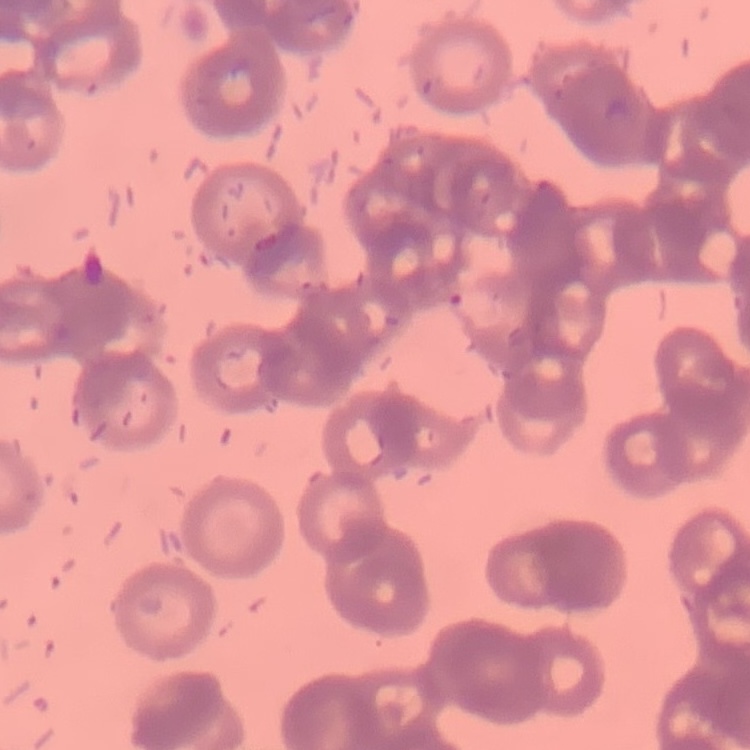
The erythrocytes exhibit rouleaux formation. Thin blood film. Field's or Giemsa stain. Square crop of a larger photomicrograph.